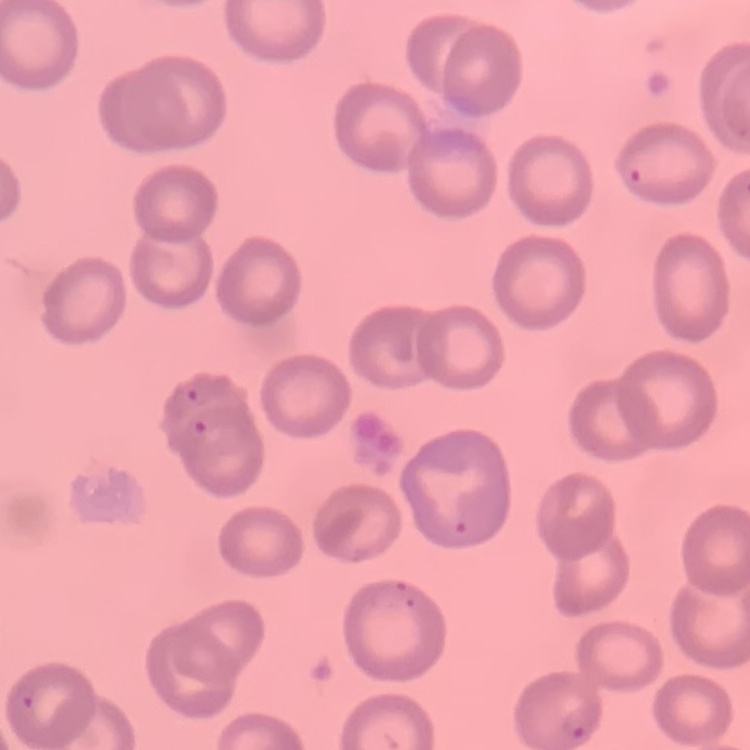

The erythrocytes exhibit no rouleaux formation. Thin peripheral smear. Stained with either Field's or Giemsa. One tile cut from a larger photomicrograph.